Outline each blood parasite and name the species.
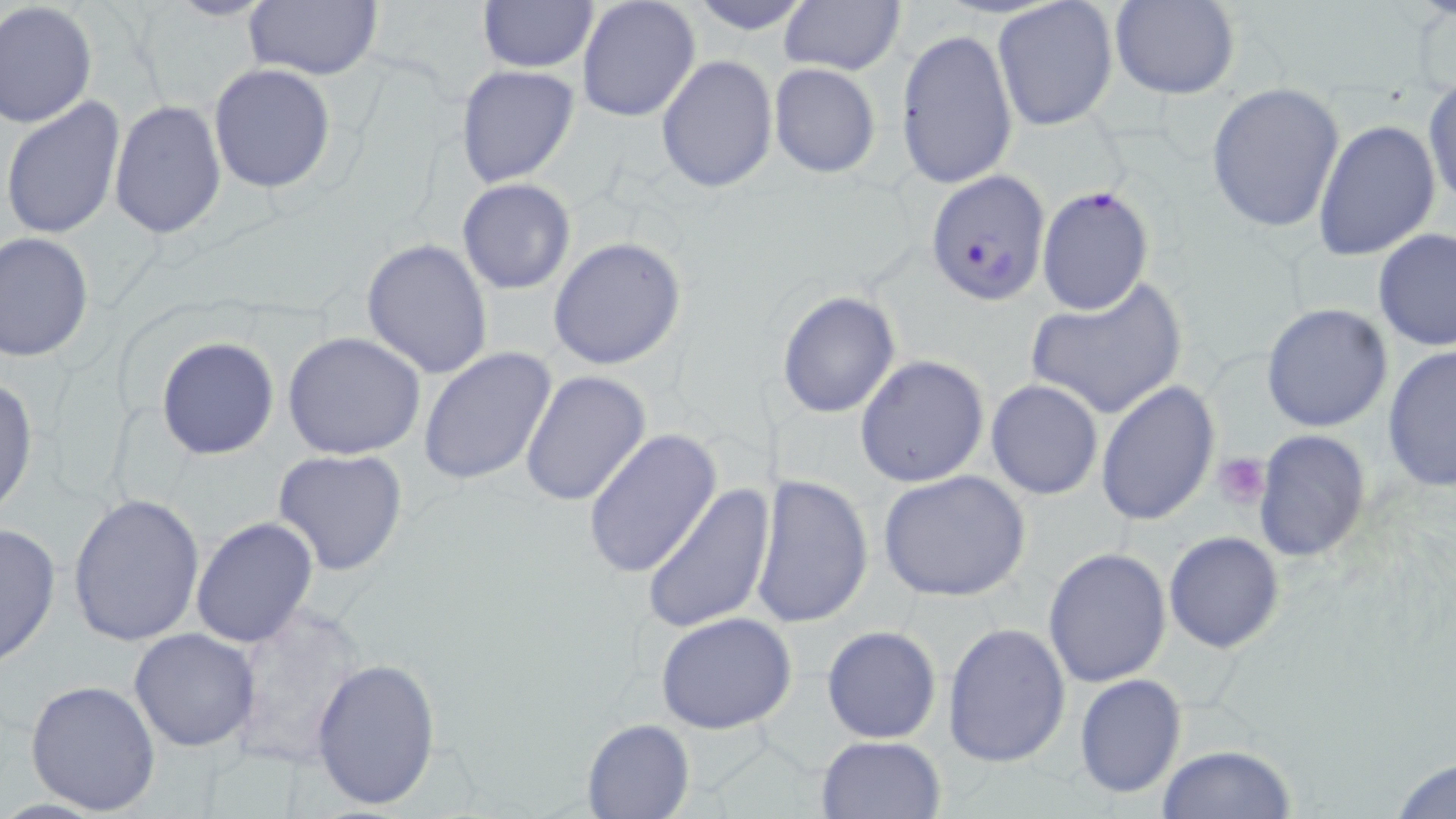
Approximate bounding boxes as (x1,y1)-(x2,y2) corner pairs in pixels.
Plasmodium falciparum-infected red blood cells: (926,170)-(1050,305), (1036,184)-(1154,316).
No Plasmodium ovale, Plasmodium malariae, Plasmodium vivax, Babesia divergens, or Trypanosoma brucei observed.

{
  "slide_level_diagnosis": "Plasmodium falciparum",
  "image_size": "1456×819 pixels",
  "platelet_locations": "approximate bounding boxes as (x1,y1)-(x2,y2) corner pairs in pixels: (1213,453)-(1270,506)",
  "stain": "May-Grünwald-Giemsa",
  "preparation": "thin blood smear",
  "modality": "optical microscopy",
  "uninfected_red_blood_cell_locations": "approximate bounding boxes as (x1,y1)-(x2,y2) corner pairs in pixels: (576,0)-(702,125), (682,0)-(818,34), (778,0)-(905,77), (475,1)-(598,75), (991,1)-(1119,132), (1112,1)-(1239,99), (242,2)-(384,82), (0,3)-(99,129), (894,25)-(1018,191), (656,55)-(778,193), (209,63)-(337,194), (767,63)-(880,177), (456,65)-(579,187), (1424,76)-(1456,215), (1205,82)-(1346,234), (2,96)-(127,241), (108,102)-(227,240), (1313,119)-(1441,261), (456,179)-(576,295), (1373,228)-(1455,350), (1,233)-(95,362), (548,236)-(687,370), (361,238)-(494,380), (1024,279)-(1187,421), (776,290)-(901,419), (1261,302)-(1393,433), (282,333)-(426,460), (156,336)-(279,460), (1381,344)-(1456,490), (419,347)-(557,487), (854,355)-(990,487), (520,369)-(651,507), (0,377)-(39,520), (985,381)-(1103,500), (1096,381)-(1219,527), (582,429)-(722,579), (1254,429)-(1371,562), (272,450)-(408,576), (876,471)-(1032,602), (749,474)-(873,628), (642,481)-(776,635), (67,493)-(205,646), (190,516)-(320,649), (0,521)-(62,669), (1163,531)-(1284,653), (1042,547)-(1172,688), (230,607)-(367,770), (656,611)-(799,735), (942,622)-(1072,768), (821,625)-(942,743), (128,629)-(260,751), (311,657)-(441,811), (1073,674)-(1186,799), (26,678)-(161,815), (582,718)-(695,818), (814,734)-(947,818), (1156,743)-(1295,818), (1387,753)-(1456,819)",
  "magnification": "1000x",
  "field_of_view": "single"
}